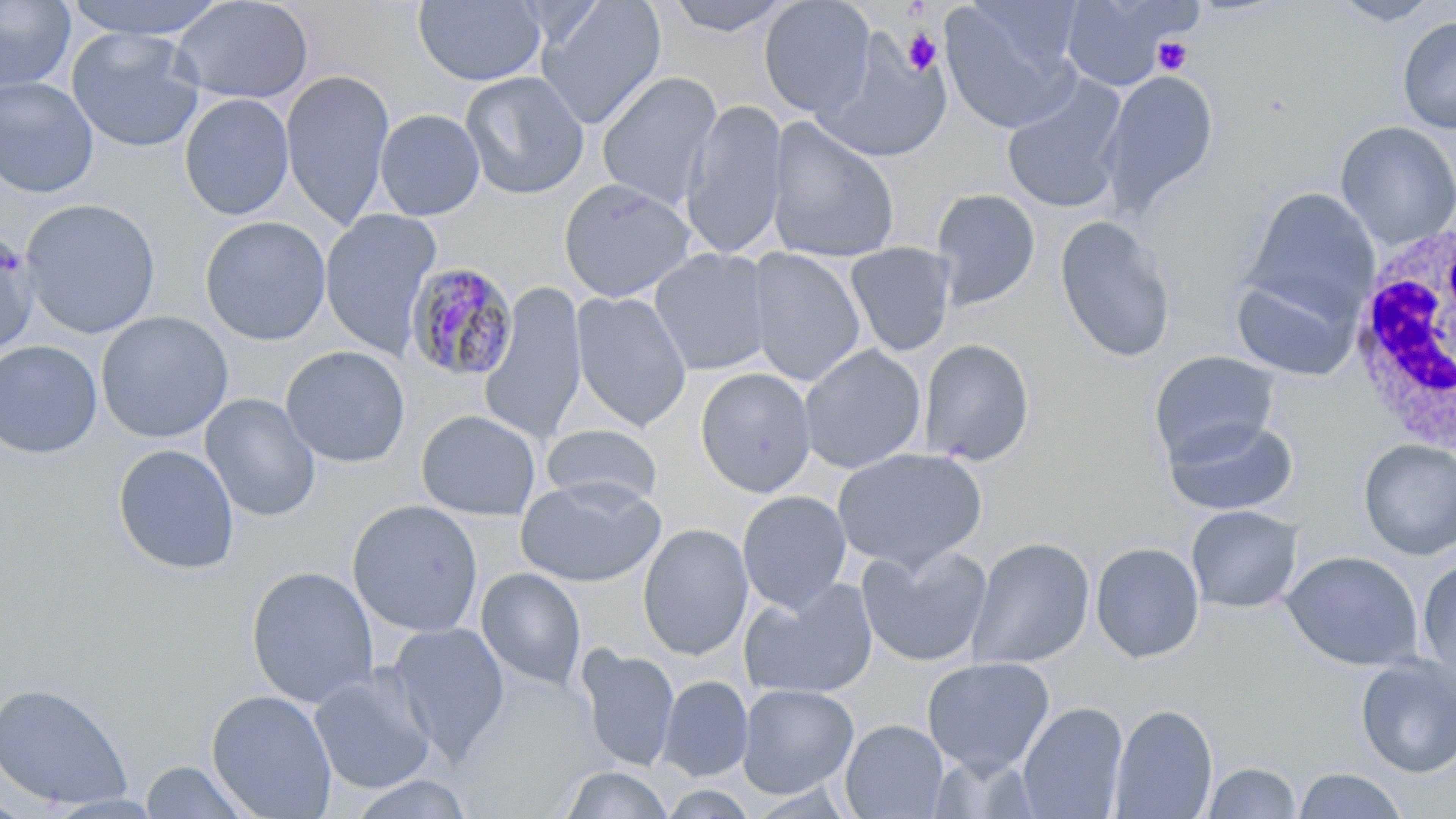

Summary:
  - Coordinate format: approximate bounding boxes as [x1, y1, x2, y2] in pixels
  - White blood cell locations: [1343, 219, 1456, 454]
  - Plasmodium malariae-infected red blood cell locations: [406, 261, 518, 382]
  - Platelet locations: [903, 30, 943, 77], [1152, 37, 1194, 76]
  - Uninfected red blood cell locations: [60, 0, 232, 40], [171, 0, 314, 105], [413, 0, 548, 87], [535, 0, 667, 130], [659, 0, 799, 38], [758, 0, 876, 119], [1058, 0, 1186, 90], [1327, 0, 1443, 26], [0, 1, 76, 91], [941, 1, 1084, 133], [1397, 16, 1456, 135], [67, 26, 205, 152], [815, 42, 954, 164], [280, 69, 395, 229], [458, 70, 590, 200], [1099, 70, 1219, 216], [596, 71, 723, 209], [1001, 75, 1128, 214], [0, 76, 99, 198], [179, 93, 294, 221], [681, 98, 788, 261], [375, 109, 486, 221], [765, 116, 901, 266], [1335, 121, 1456, 250], [558, 178, 699, 303], [1242, 187, 1379, 320], [931, 188, 1041, 310], [20, 198, 161, 339], [319, 209, 441, 358], [1054, 214, 1176, 364], [200, 215, 331, 345], [0, 229, 40, 358], [844, 242, 956, 357], [743, 247, 866, 387], [648, 248, 775, 376], [1230, 271, 1362, 381], [479, 283, 587, 446], [570, 290, 693, 432], [95, 310, 233, 443], [918, 338, 1035, 466], [0, 340, 103, 459], [799, 344, 926, 473], [280, 345, 411, 468], [1149, 350, 1279, 465], [695, 368, 816, 498], [200, 393, 321, 523], [416, 409, 541, 521], [1162, 415, 1299, 516], [540, 424, 664, 510], [1358, 439, 1456, 560], [113, 443, 239, 575], [831, 447, 987, 573], [515, 478, 665, 587], [737, 490, 852, 613], [347, 499, 484, 638], [1186, 505, 1302, 613], [638, 523, 754, 661], [967, 537, 1094, 670], [1089, 542, 1204, 663], [857, 545, 993, 667], [1282, 551, 1422, 670], [1416, 558, 1456, 682], [245, 565, 378, 708], [475, 568, 587, 691], [740, 578, 877, 701], [388, 622, 510, 762], [577, 645, 679, 773], [1355, 655, 1456, 778], [921, 656, 1055, 774], [309, 666, 438, 795], [658, 675, 753, 782], [0, 683, 132, 810], [737, 683, 859, 798], [206, 689, 337, 818], [1017, 702, 1128, 819], [1109, 705, 1218, 818], [840, 719, 948, 818], [138, 760, 255, 819], [1202, 761, 1301, 818], [560, 766, 676, 818], [1292, 768, 1409, 819]
  - Slide-level diagnosis: Plasmodium malariae
  - Field of view: single
  - Modality: optical microscopy
  - Magnification: 1000x
  - Preparation: thin blood film
  - Stain: May-Grünwald-Giemsa
  - Image size: 1456×819 pixels